Describe the morphology of the red blood cells.
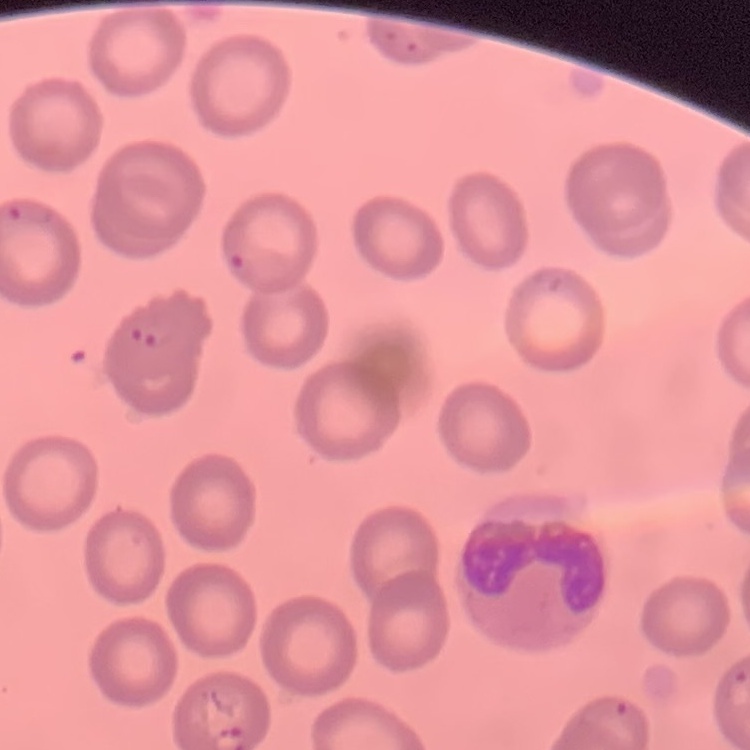

No rouleaux formation.

Square crop of a larger photomicrograph. Thin peripheral smear. Stained with either Field's or Giemsa.